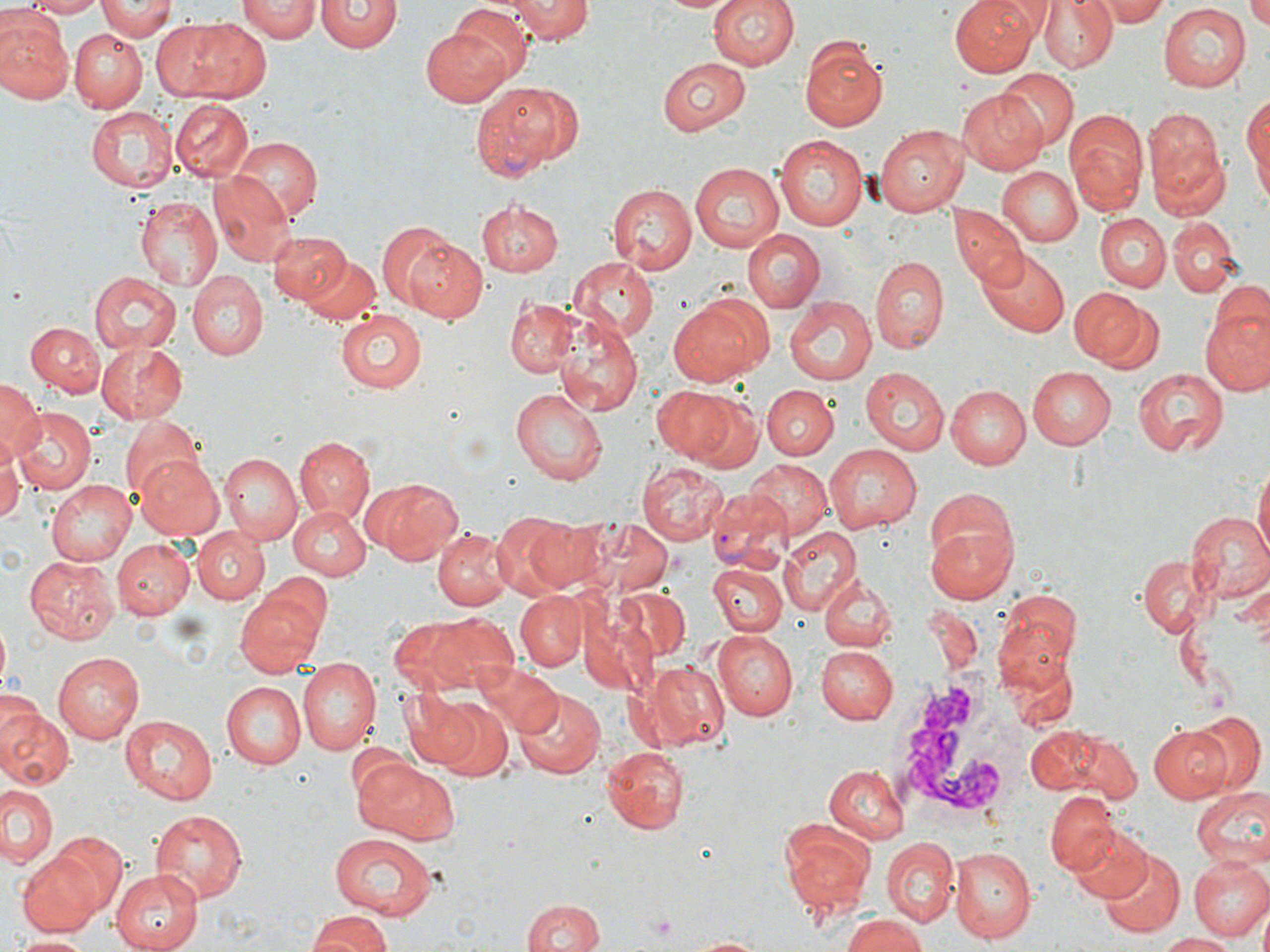

slide-level diagnosis = Plasmodium vivax
field of view = one of a larger specimen
white blood cell locations = approximate bounding boxes as (x1, y1, x2, y2) in pixels: (891, 666, 1026, 833)
Plasmodium vivax-infected red blood cell locations = approximate bounding boxes as (x1, y1, x2, y2) in pixels: (469, 82, 577, 180), (707, 487, 794, 572)
modality = optical microscopy
stain = May-Grünwald-Giemsa
uninfected red blood cell locations = approximate bounding boxes as (x1, y1, x2, y2) in pixels: (18, 0, 102, 15), (239, 0, 318, 43), (509, 0, 590, 46), (654, 0, 735, 14), (705, 0, 800, 74), (949, 0, 1037, 75), (1039, 0, 1118, 74), (1244, 0, 1270, 31), (96, 1, 178, 41), (317, 1, 400, 54), (1094, 1, 1174, 25), (1157, 4, 1250, 91), (451, 5, 534, 82), (0, 15, 72, 105), (153, 18, 273, 102), (423, 24, 517, 105), (68, 29, 146, 113), (799, 35, 890, 134), (657, 56, 752, 135), (998, 68, 1078, 152), (959, 88, 1049, 175), (1243, 94, 1269, 199), (171, 98, 255, 183), (85, 106, 177, 192), (1143, 109, 1225, 200), (1065, 111, 1147, 217), (875, 124, 973, 215), (773, 133, 870, 231), (230, 137, 322, 224), (1151, 145, 1230, 223), (689, 161, 786, 249), (996, 165, 1083, 247), (209, 173, 293, 266), (609, 181, 698, 274), (136, 196, 224, 292), (474, 199, 561, 278), (951, 208, 1028, 289), (1094, 212, 1172, 291), (1170, 221, 1237, 295), (375, 222, 456, 309), (742, 228, 826, 311), (267, 230, 351, 305), (403, 238, 485, 323), (974, 247, 1070, 336), (300, 254, 383, 328), (870, 255, 950, 356), (568, 257, 657, 341), (186, 270, 268, 358), (89, 273, 179, 354), (1207, 282, 1270, 352), (1069, 286, 1148, 367), (668, 294, 771, 387), (784, 295, 878, 386), (505, 298, 579, 377), (1094, 301, 1167, 376), (1201, 306, 1270, 393), (333, 309, 429, 395), (552, 314, 644, 416), (27, 321, 105, 393), (35, 326, 175, 410), (96, 342, 188, 424), (1026, 365, 1115, 449), (860, 368, 949, 455), (1132, 368, 1226, 458), (0, 380, 44, 460), (762, 384, 838, 459), (946, 384, 1031, 468), (654, 386, 744, 466), (510, 387, 609, 486), (11, 406, 94, 495), (117, 413, 205, 500), (293, 435, 376, 525), (0, 442, 22, 528), (823, 443, 926, 533), (134, 454, 226, 540), (219, 454, 301, 546), (744, 459, 834, 541), (638, 460, 728, 544), (1253, 463, 1269, 571), (373, 478, 464, 564), (44, 480, 135, 565), (288, 506, 370, 579), (1185, 511, 1270, 602), (491, 512, 575, 594), (520, 516, 607, 592), (571, 518, 675, 595), (927, 522, 1019, 603), (779, 525, 862, 616), (192, 527, 269, 604), (432, 528, 513, 611), (110, 540, 194, 618), (1136, 553, 1211, 636), (25, 554, 118, 644), (708, 561, 787, 637), (266, 571, 332, 646), (822, 572, 896, 651), (616, 587, 691, 660), (234, 588, 327, 676), (999, 590, 1081, 672), (515, 592, 586, 670), (420, 614, 518, 694), (710, 629, 798, 721), (816, 645, 899, 725), (54, 652, 144, 741), (297, 658, 381, 757), (642, 658, 730, 752), (473, 661, 563, 736), (219, 680, 304, 769), (512, 687, 606, 780), (403, 698, 478, 771), (433, 700, 512, 781), (0, 706, 74, 790), (1188, 710, 1265, 796), (119, 715, 217, 806), (1022, 720, 1138, 805), (1148, 724, 1232, 803), (601, 745, 690, 834), (351, 756, 455, 845), (823, 763, 910, 843), (2, 784, 60, 868), (1191, 784, 1268, 876), (1045, 791, 1119, 874), (149, 807, 249, 902), (781, 817, 881, 919), (1065, 821, 1154, 903), (46, 832, 128, 917), (328, 834, 440, 918), (880, 836, 957, 925), (947, 843, 1037, 943), (1098, 846, 1186, 938), (16, 852, 105, 937), (1188, 854, 1270, 941), (112, 868, 207, 952), (520, 898, 605, 952), (306, 910, 393, 952), (840, 913, 933, 952), (1156, 933, 1240, 951), (13, 934, 93, 951), (683, 935, 773, 952)
platelet locations = approximate bounding boxes as (x1, y1, x2, y2) in pixels: (645, 913, 679, 937)
magnification = 1000x
preparation = thin blood film
image size = 1270×952 pixels